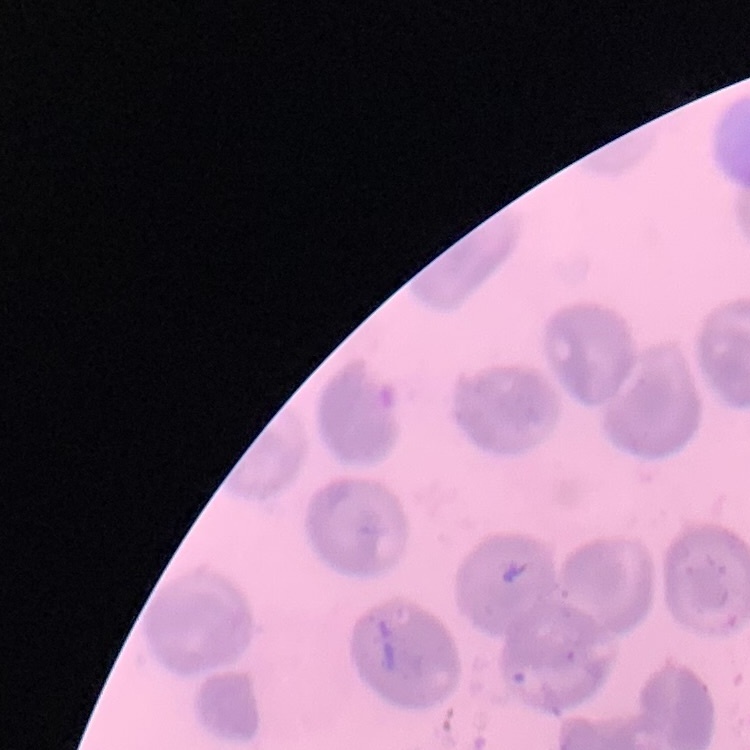

Summary:
  - Erythrocyte morphology: no rouleaux formation
  - Image type: one tile cut from a larger photomicrograph
  - Preparation: thin peripheral smear
  - Stain: Field's or Giemsa